Name the parasite shown.
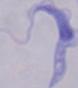
This is a trypanosome.

Summary:
  - Magnification: 1000x
  - Modality: micrograph